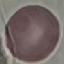

{
  "result": "no malaria parasites detected",
  "capture": "smartphone camera at the microscope eyepiece",
  "preparation": "thin blood film",
  "stain": "Giemsa",
  "image_type": "automatically extracted cell patch, resized to 64 × 64 pixels"
}